Assess this cell for malaria.
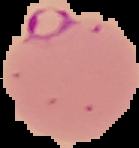

Parasitized.

Summary:
  - Image type: cell region segmented out of the field of view; surrounding area masked to black
  - Image size: 139×148 pixels
  - Preparation: thin blood smear